Assess this cell for malaria.
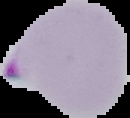
Parasitized.

From a thin blood smear. Image is 130×118 pixels. The area outside the segmented cell region is set to black.